Comment on the morphology of the erythrocytes.
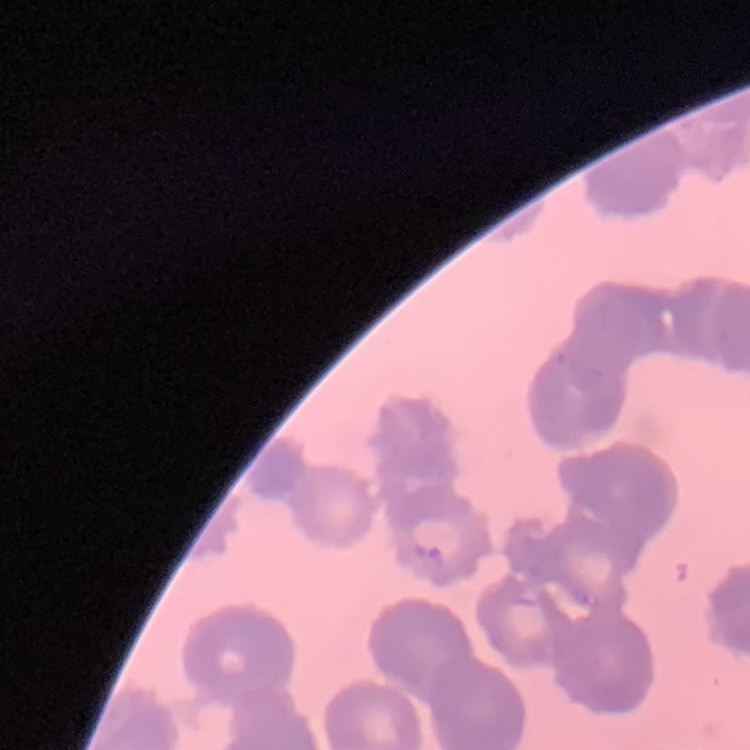

They show rouleaux formation.

Summary:
  - Preparation: thin blood smear
  - Stain: Field's or Giemsa
  - Image type: one tile cut from a larger photomicrograph